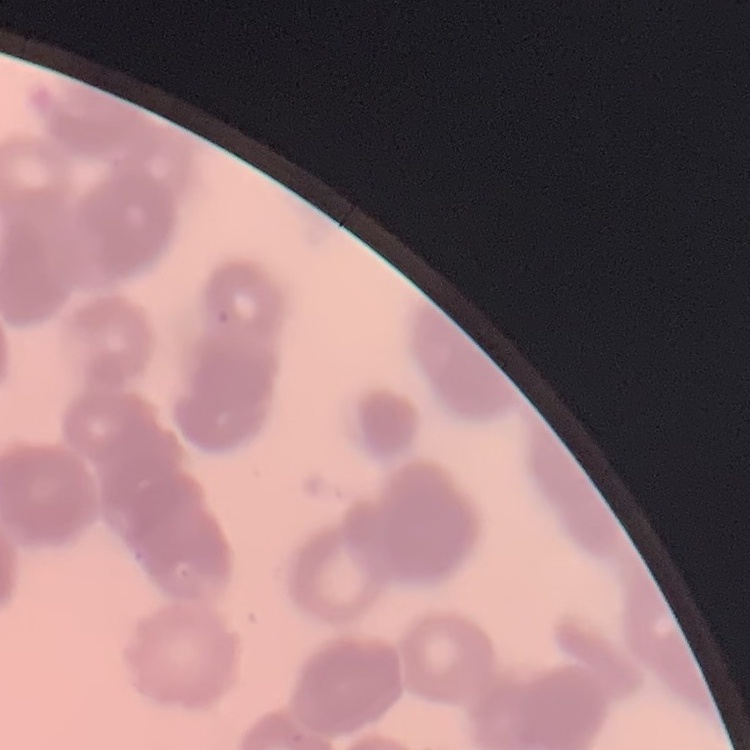 The erythrocytes show rouleaux formation. Stained with either Field's or Giemsa. One tile cut from a larger photomicrograph. Thin peripheral smear.